Point out each Plasmodium parasite.
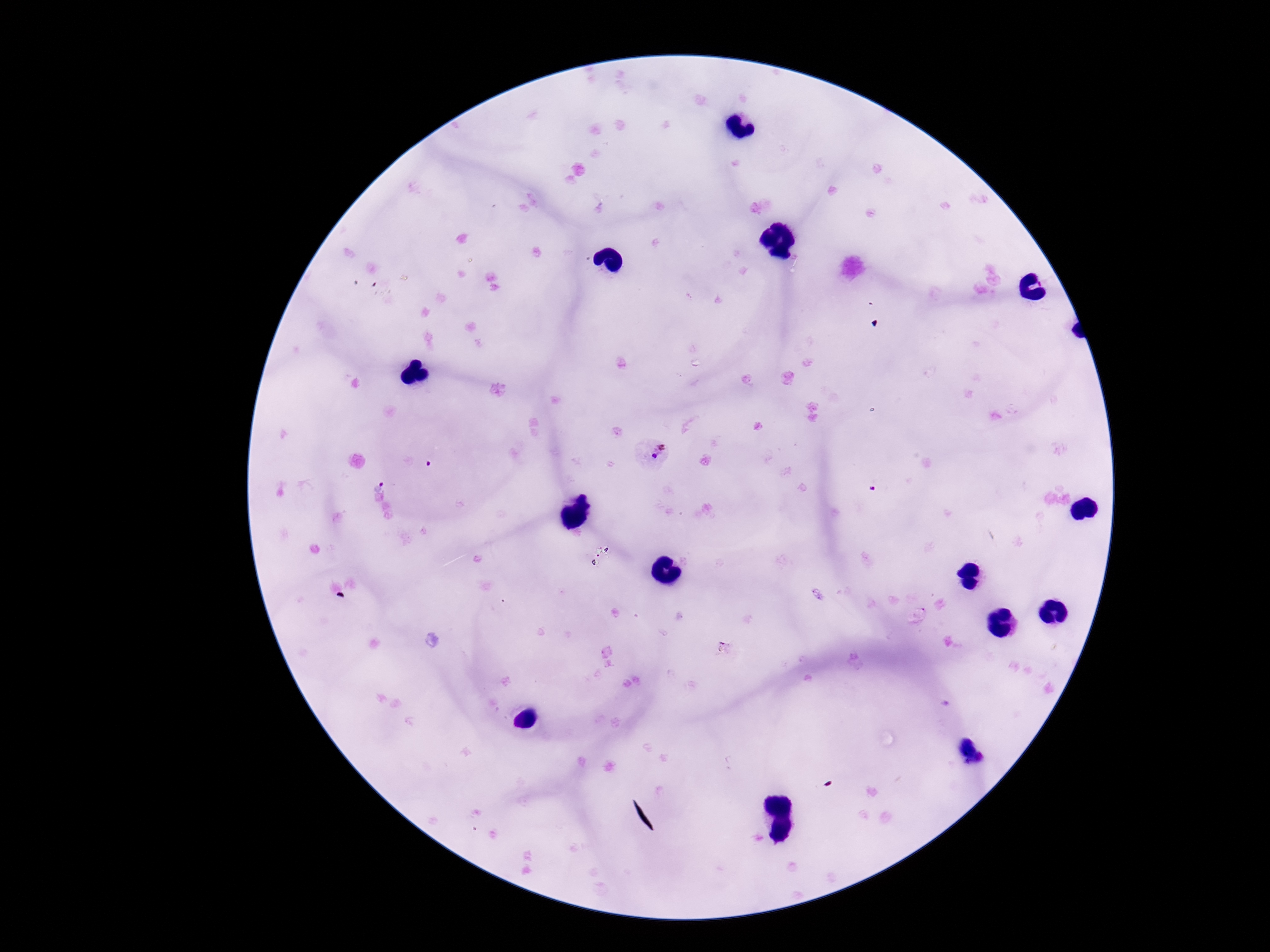
Approximate centers as {x, y} in pixels.
Plasmodium parasites: {653, 452}, {378, 480}.

Summary:
  - Preparation: thick blood smear
  - Stain: Giemsa
  - Capture: smartphone camera through the microscope eyepiece
  - Patient malaria status: infected
  - Field of view: single
  - Image size: 1270×952 pixels
  - Magnification: 100x